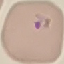

result: malaria parasites detected
capture: smartphone through the microscope eyepiece
image_type: cell patch, automatically extracted from a larger field of view and resized to 64 × 64 pixels
preparation: thin blood film
stain: Giemsa